Name the blood parasite species.
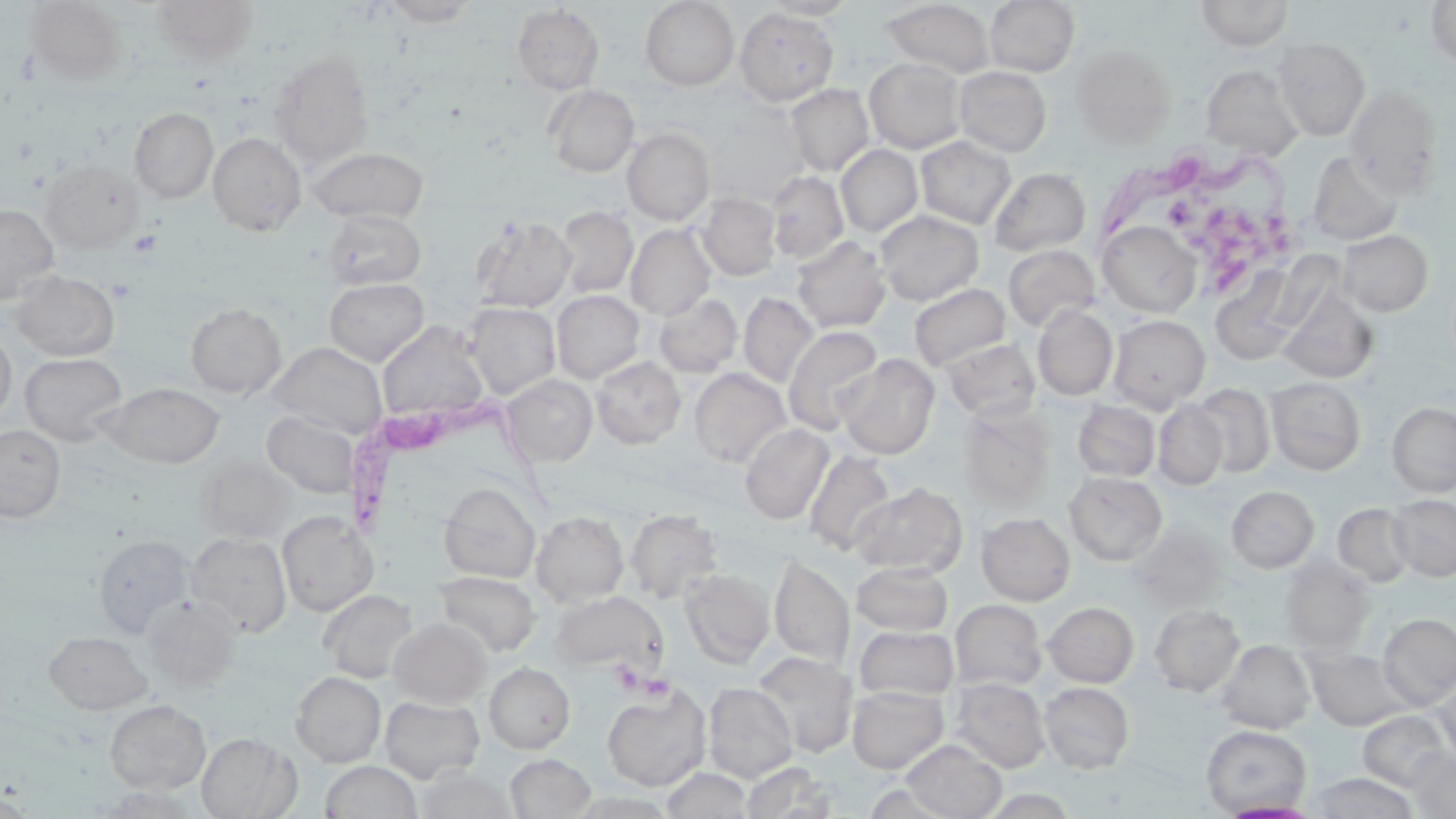
Trypanosoma brucei.

Summary:
  - Coordinate format: approximate bounding boxes as (x1, y1, x2, y2) in pixels
  - Trypanosoma brucei locations: (1089, 133, 1295, 249), (340, 387, 555, 541)
  - Uninfected red blood cell locations: (151, 0, 259, 65), (381, 0, 479, 26), (639, 0, 739, 90), (984, 0, 1080, 76), (1194, 0, 1294, 51), (1425, 0, 1456, 72), (24, 1, 128, 85), (761, 1, 859, 19), (884, 1, 994, 77), (512, 4, 605, 95), (735, 8, 839, 104), (1273, 37, 1370, 141), (1070, 44, 1176, 148), (269, 51, 375, 166), (864, 57, 967, 153), (1201, 64, 1303, 160), (954, 66, 1052, 157), (785, 83, 874, 176), (544, 84, 639, 177), (1344, 85, 1443, 198), (129, 107, 218, 203), (621, 127, 715, 226), (207, 132, 306, 237), (916, 136, 1016, 229), (835, 145, 922, 237), (309, 147, 429, 225), (1307, 151, 1404, 246), (39, 159, 142, 254), (989, 168, 1091, 257), (767, 172, 848, 264), (698, 192, 781, 280), (0, 203, 59, 305), (555, 206, 638, 298), (323, 209, 425, 290), (875, 210, 984, 305), (471, 215, 576, 313), (1098, 221, 1202, 317), (625, 223, 716, 320), (1337, 230, 1433, 316), (792, 236, 891, 333), (1003, 244, 1100, 332), (1210, 266, 1305, 365), (10, 269, 120, 360), (324, 278, 429, 365), (909, 283, 1011, 370), (1279, 287, 1379, 384), (552, 290, 644, 383), (654, 292, 743, 377), (738, 292, 819, 388), (464, 302, 561, 399), (185, 303, 286, 398), (1033, 304, 1118, 400), (1108, 315, 1209, 411), (378, 323, 489, 422), (783, 325, 884, 435), (0, 326, 16, 426), (941, 338, 1041, 422), (268, 342, 387, 437), (20, 353, 127, 446), (837, 354, 940, 459), (591, 356, 685, 448), (689, 368, 791, 467), (502, 374, 597, 466), (1267, 377, 1366, 475), (103, 382, 224, 468), (1190, 383, 1276, 478), (1072, 400, 1160, 482), (1154, 400, 1228, 489), (1388, 402, 1456, 497), (958, 406, 1055, 506), (262, 410, 362, 499), (740, 423, 834, 524), (0, 425, 66, 522), (804, 450, 896, 555), (196, 456, 292, 543), (1065, 472, 1167, 565), (438, 482, 541, 583), (850, 482, 968, 576), (1227, 486, 1319, 572), (1388, 494, 1456, 581), (1334, 503, 1415, 587), (625, 509, 723, 603), (276, 510, 378, 617), (532, 511, 629, 606), (977, 512, 1075, 605), (1129, 524, 1228, 611), (187, 532, 292, 636), (93, 534, 195, 636), (769, 552, 855, 668), (1279, 557, 1374, 651), (852, 563, 953, 635), (680, 569, 775, 667), (435, 571, 540, 656), (318, 589, 417, 682), (550, 590, 667, 676), (140, 595, 242, 689), (950, 599, 1047, 690), (1043, 601, 1139, 687), (1149, 604, 1245, 696), (1378, 613, 1456, 709), (389, 618, 490, 707), (855, 625, 959, 701), (44, 631, 152, 714), (1217, 639, 1315, 734), (1306, 648, 1411, 731), (752, 651, 858, 758), (484, 663, 575, 754), (291, 671, 386, 767), (1434, 677, 1456, 767), (951, 678, 1050, 773), (703, 682, 797, 782), (1039, 682, 1135, 773), (603, 684, 710, 790), (847, 685, 948, 773), (379, 695, 484, 783), (104, 700, 211, 794), (1357, 710, 1453, 791), (1200, 724, 1312, 816), (197, 731, 301, 818), (900, 739, 1006, 818), (1408, 749, 1456, 818), (505, 754, 596, 818), (320, 761, 422, 819), (742, 762, 841, 818), (415, 767, 517, 819), (663, 767, 751, 818), (1309, 772, 1419, 819), (1, 792, 34, 817), (1217, 800, 1320, 818)
  - Platelet locations: (1170, 198, 1292, 282)
  - Stain: May-Grünwald-Giemsa
  - Preparation: thin blood smear
  - Magnification: 1000x
  - Modality: optical microscopy
  - Field of view: one of a larger specimen
  - Image size: 1456×819 pixels